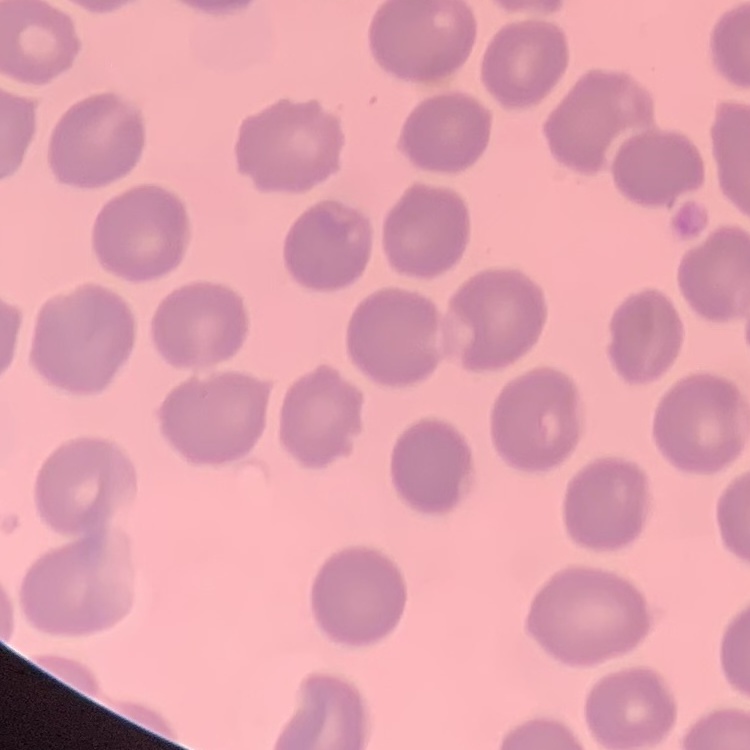

The red blood cells show no rouleaux formation. Thin peripheral smear. Stained with either Field's or Giemsa. Square crop of a larger photomicrograph.